Classify this cell by malaria status.
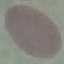
Uninfected.

image_type: automatically extracted cell patch, resized to 64 × 64 pixels
preparation: thin blood film
capture: smartphone through the microscope eyepiece
stain: Giemsa